Report the malaria status of this cell.
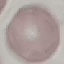
Uninfected.

image_type: automatically extracted cell patch, resized to 64 × 64 pixels
preparation: thin blood film
stain: Giemsa
capture: smartphone camera at the microscope eyepiece